State which parasite is depicted.
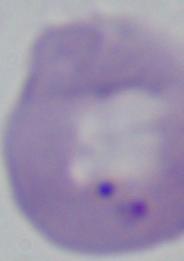
Babesia.

Summary:
  - Modality: micrograph
  - Magnification: 1000x